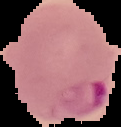
The area outside the segmented cell region is set to black. Image is 121×127 pixels. Result: malaria parasites identified. From a thin blood smear.